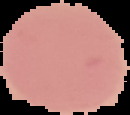

result: no Plasmodium parasites seen
image_size: 130×115 pixels
preparation: thin blood film
image_type: cell region segmented out of the field of view; surrounding area masked to black